Give the location of every parasitized RBC.
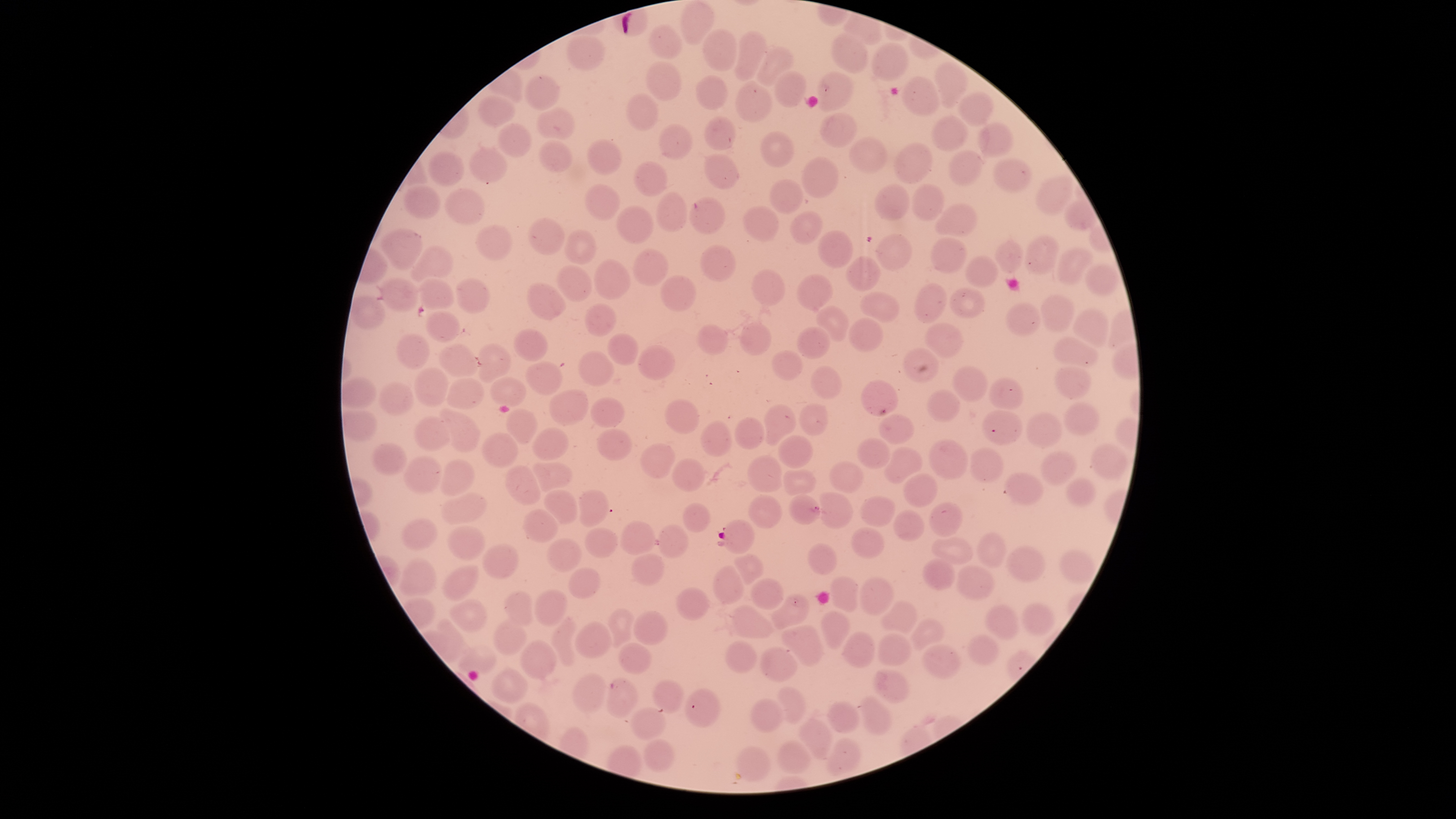

Approximate bounding boxes as [left, top, right, bottom] in pixels.
Parasitized RBCs: [717, 518, 755, 554].

Approximate bounding boxes as [left, top, right, bottom] in pixels.
Summary:
  - Uninfected RBCs: [679, 1, 714, 43], [647, 25, 681, 59], [702, 30, 737, 71], [734, 32, 768, 81], [831, 34, 868, 74], [565, 35, 606, 71], [870, 43, 909, 79], [755, 49, 793, 85], [934, 60, 967, 107], [646, 61, 682, 102], [775, 69, 807, 109], [817, 71, 853, 112], [524, 75, 559, 111], [695, 75, 729, 110], [902, 76, 943, 117], [735, 83, 773, 122], [958, 92, 995, 126], [625, 94, 658, 130], [477, 95, 515, 126], [538, 107, 574, 139], [820, 112, 854, 148], [931, 115, 967, 153], [704, 116, 735, 151], [657, 123, 694, 160], [978, 123, 1014, 159], [498, 124, 530, 157], [760, 130, 795, 167], [851, 137, 886, 173], [539, 139, 573, 174], [587, 139, 621, 176], [894, 143, 933, 183], [468, 146, 508, 183], [947, 150, 985, 186], [429, 152, 466, 186], [705, 154, 740, 189], [801, 157, 839, 197], [992, 158, 1033, 193], [633, 162, 667, 197], [1035, 174, 1074, 216], [770, 180, 803, 215], [402, 184, 441, 220], [584, 184, 623, 221], [911, 184, 945, 221], [874, 185, 909, 220], [444, 189, 487, 225], [655, 191, 688, 231], [688, 198, 726, 234], [934, 203, 978, 236], [616, 205, 654, 245], [741, 207, 780, 242], [790, 211, 823, 244], [526, 217, 566, 254], [476, 224, 512, 260], [379, 229, 424, 270], [565, 230, 597, 264], [817, 230, 855, 267], [875, 233, 912, 271], [1024, 235, 1061, 275], [930, 236, 968, 273], [995, 241, 1023, 274], [700, 243, 735, 282], [410, 246, 452, 281], [1057, 248, 1094, 285], [632, 249, 669, 284], [965, 255, 999, 289], [846, 257, 882, 292], [594, 259, 630, 301], [555, 265, 593, 302], [1085, 268, 1121, 295], [751, 269, 785, 306], [797, 273, 831, 312], [661, 275, 696, 311], [382, 278, 418, 312], [456, 278, 490, 313], [419, 279, 453, 309], [525, 282, 565, 320], [914, 283, 947, 323], [950, 287, 987, 320], [859, 293, 899, 321], [1040, 294, 1075, 333], [349, 296, 385, 328], [1006, 301, 1041, 337], [583, 304, 618, 338], [817, 306, 847, 340], [1073, 308, 1109, 348], [425, 310, 461, 342], [848, 318, 884, 352], [925, 322, 963, 358], [694, 323, 728, 354], [739, 323, 770, 355], [795, 327, 831, 360], [512, 329, 549, 362], [607, 333, 638, 365], [396, 334, 430, 369], [1052, 337, 1098, 365], [439, 344, 477, 377], [478, 344, 511, 384], [637, 344, 675, 380], [902, 347, 939, 383], [580, 351, 614, 387], [772, 351, 804, 380], [526, 362, 563, 395], [810, 366, 844, 401], [952, 366, 989, 402], [414, 367, 449, 407], [1055, 367, 1092, 400], [445, 376, 484, 410], [490, 377, 528, 407], [989, 377, 1025, 410], [861, 380, 899, 417], [378, 382, 415, 416], [550, 389, 588, 425], [925, 389, 961, 423], [591, 397, 625, 428], [664, 399, 701, 434], [1064, 401, 1099, 436], [799, 403, 831, 437], [764, 405, 796, 446], [507, 408, 539, 445], [437, 409, 482, 453], [982, 410, 1023, 445], [1026, 412, 1064, 448], [879, 414, 915, 444], [413, 416, 450, 450], [735, 417, 764, 451], [699, 420, 731, 458], [531, 428, 568, 462], [596, 429, 631, 462], [484, 432, 518, 467], [777, 436, 813, 469], [857, 437, 891, 469], [929, 440, 969, 479], [1090, 441, 1126, 480], [371, 443, 406, 474], [639, 444, 673, 480], [885, 446, 923, 484], [969, 448, 1004, 482], [1041, 451, 1077, 487], [747, 456, 784, 492], [404, 457, 443, 494], [672, 457, 706, 492], [437, 460, 475, 497], [828, 461, 863, 493], [533, 462, 572, 493], [506, 465, 540, 505], [783, 469, 817, 496], [1004, 473, 1044, 507], [903, 474, 938, 508], [1067, 478, 1095, 509], [545, 490, 578, 525], [577, 490, 609, 526], [818, 492, 852, 528], [442, 493, 487, 525], [748, 495, 783, 529], [789, 495, 821, 524], [860, 498, 896, 527], [682, 502, 710, 533], [929, 503, 962, 536], [891, 508, 924, 543], [522, 509, 557, 544], [400, 517, 437, 551], [622, 519, 655, 556], [660, 524, 688, 558], [447, 525, 487, 561], [851, 527, 885, 557], [585, 528, 618, 558], [976, 532, 1006, 568], [547, 538, 582, 573], [931, 538, 972, 566], [808, 543, 837, 576], [482, 544, 518, 579], [1008, 545, 1044, 582], [1058, 549, 1097, 585], [631, 553, 665, 586], [735, 554, 764, 583], [398, 558, 437, 596], [922, 559, 954, 591], [442, 564, 478, 603], [957, 564, 995, 601], [714, 566, 744, 604], [567, 568, 602, 600], [829, 576, 858, 611], [859, 577, 894, 616], [750, 578, 784, 608], [676, 587, 710, 621], [534, 588, 568, 627], [503, 590, 534, 625], [771, 595, 810, 628], [450, 599, 487, 633], [881, 600, 916, 634], [1022, 603, 1055, 636], [982, 604, 1018, 642], [731, 605, 777, 640], [608, 607, 635, 646], [633, 611, 666, 645], [821, 611, 849, 648], [552, 614, 577, 666], [437, 618, 471, 656], [493, 619, 528, 656], [911, 619, 944, 649], [574, 620, 609, 658], [779, 626, 824, 667], [844, 631, 874, 669], [877, 634, 913, 665], [967, 634, 1000, 664], [521, 640, 556, 680], [724, 641, 756, 674], [615, 642, 650, 674], [922, 643, 962, 680], [458, 644, 497, 674], [760, 646, 798, 683], [493, 666, 529, 703], [874, 670, 908, 703], [571, 672, 604, 714], [606, 678, 638, 719], [651, 679, 685, 713], [778, 685, 805, 724], [685, 688, 722, 728], [862, 697, 891, 734], [749, 698, 782, 733], [828, 702, 859, 732], [630, 706, 665, 739], [799, 720, 833, 758], [826, 737, 860, 775], [644, 738, 675, 771], [776, 740, 813, 775], [735, 744, 772, 781]
  - Stain: Giemsa
  - Field of view: single
  - Species: Plasmodium falciparum
  - Visible region: circular
  - Preparation: thin smear of blood
  - Capture: smartphone photograph through the microscope eyepiece
  - Image size: 1456×819 pixels